Give the position of each Plasmodium falciparum parasite with its life-cycle stage, each leukocyte, and any debris.
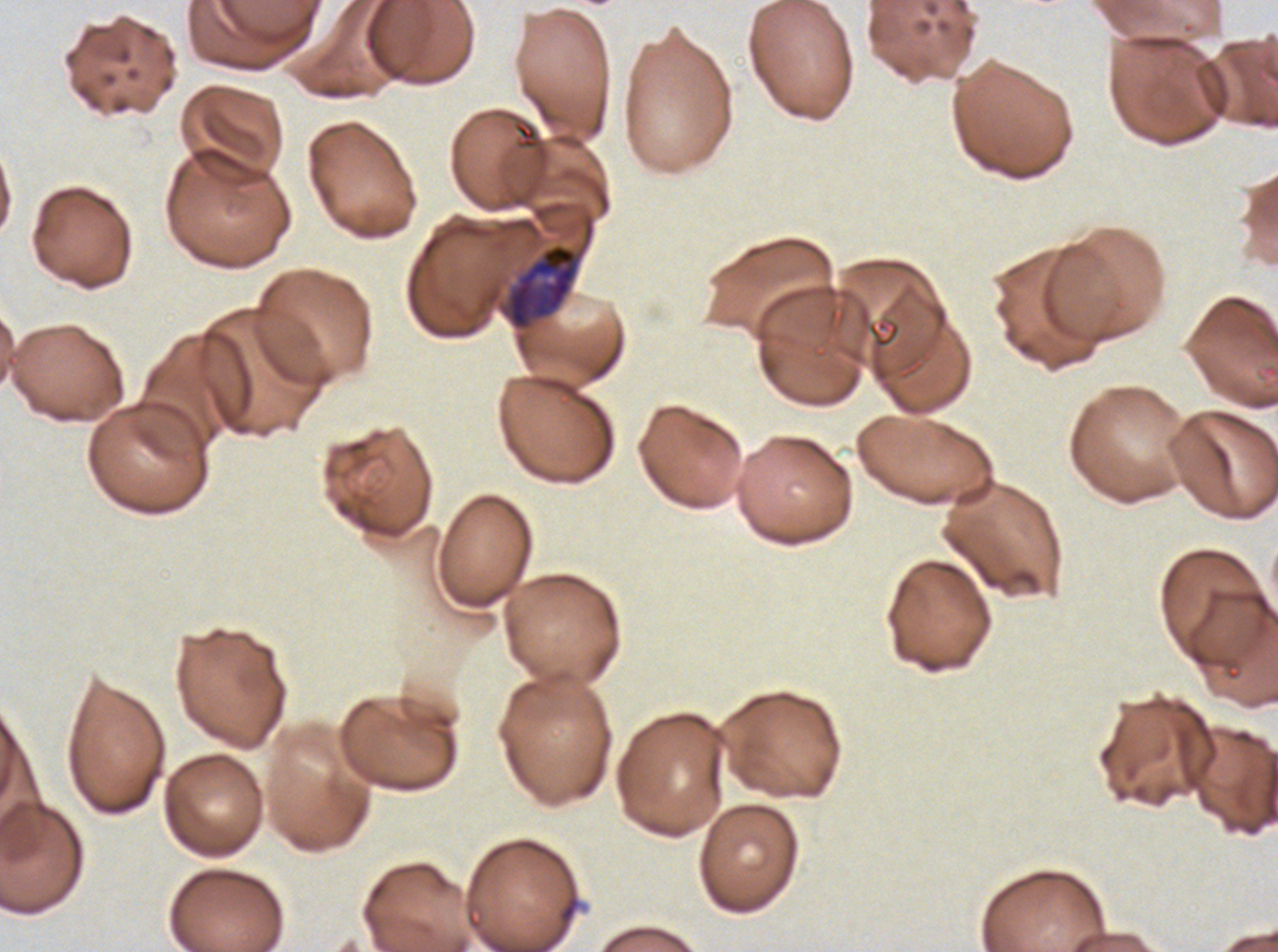

Approximate bounding boxes as [x1, y1, x2, y2] in pixels.
Late trophozoites: [506, 243, 579, 330].
No rings, late-ring/early-trophozoite forms, mid trophozoites, early schizonts, late schizonts, segmenters, gametocytes, leukocytes, or debris observed.

stain = Giemsa
specimen = Plasmodium falciparum from a patient in The Gambia, cultured ex vivo for 24 to 48 hours
preparation = thin blood film
image size = 1278×952 pixels
field of view = one sub-image of a larger composite